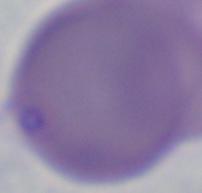

Summary:
  - Identification: Babesia
  - Magnification: 1000x
  - Modality: micrograph